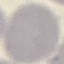
Summary:
  - Result: no malaria parasites detected
  - Stain: Giemsa
  - Image type: cell patch, automatically extracted from a larger field of view and resized to 64 × 64 pixels
  - Capture: smartphone through the microscope eyepiece
  - Preparation: thin blood smear